Comment on the morphology of the red blood cells.
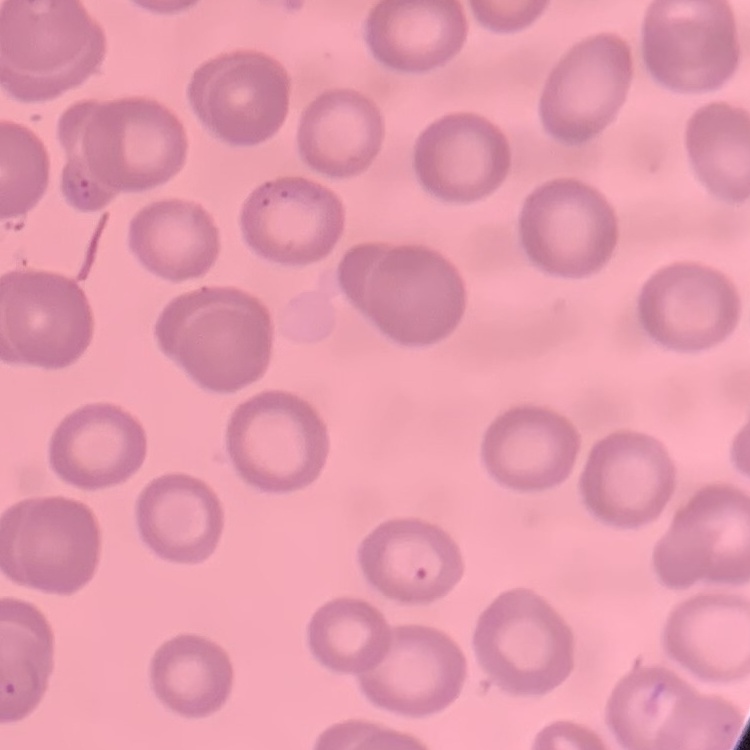
They show no rouleaux formation.

One tile cut from a larger photomicrograph. Thin blood smear. Field's or Giemsa stain.